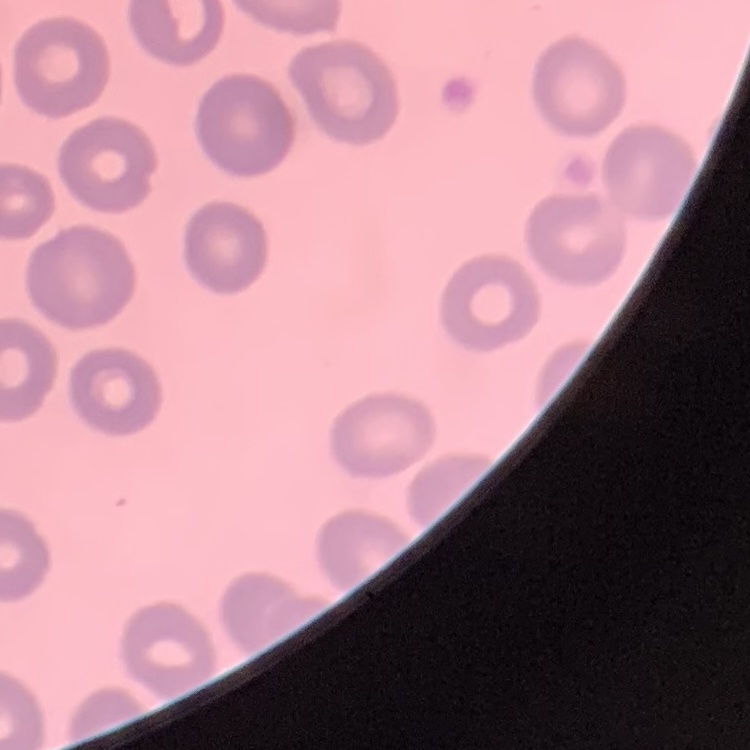

red blood cell morphology = no rouleaux formation
preparation = thin blood smear
image type = square crop of a larger photomicrograph
stain = Field's or Giemsa